Assess this cell for malaria.
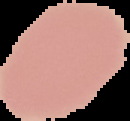

Uninfected.

From a thin blood smear. The area outside the segmented cell region is set to black. Image is 130×121 pixels.